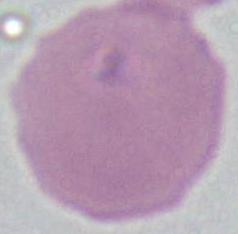

A red blood cell is shown. Photomicrograph. Captured at 1000x magnification.